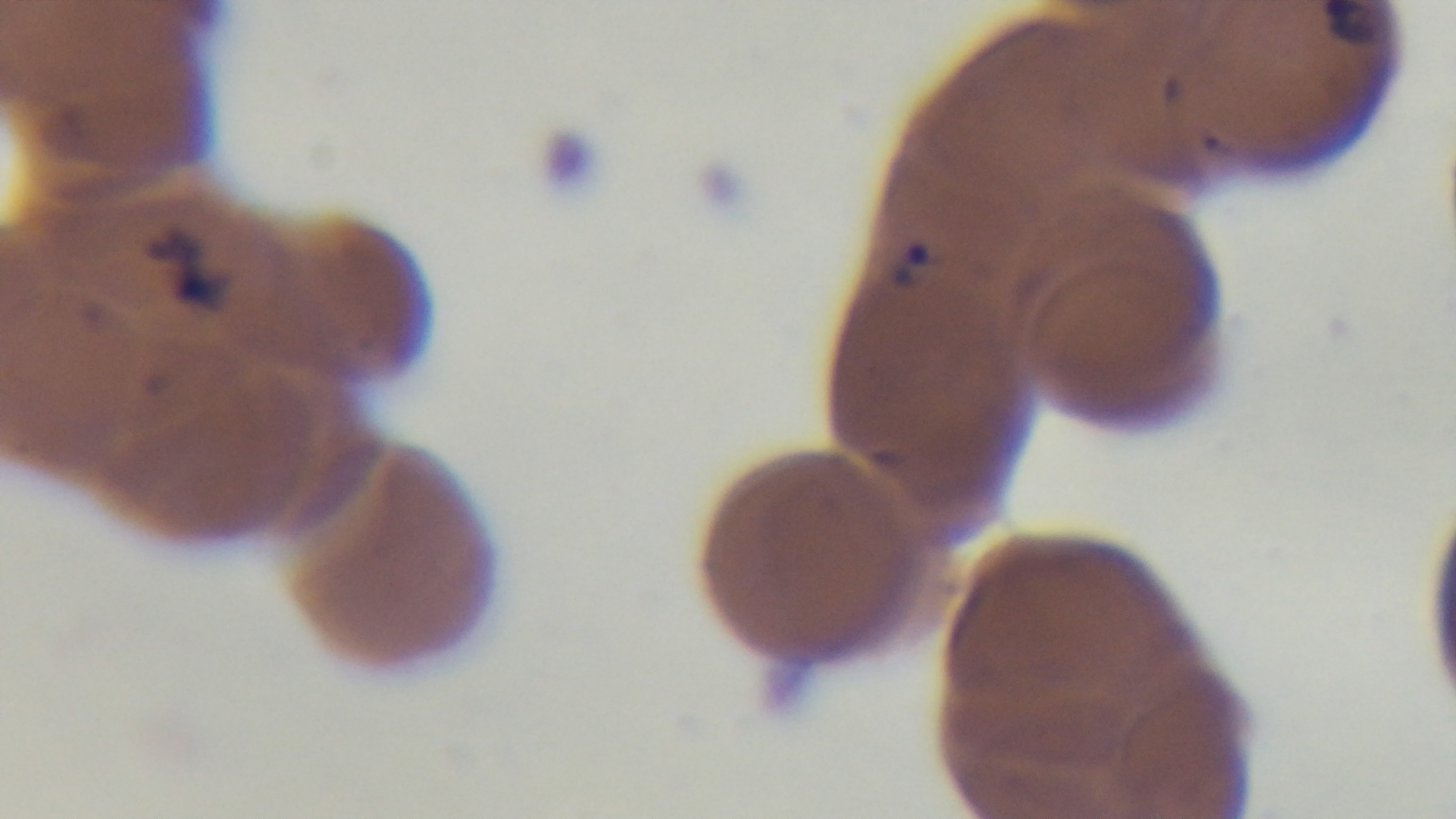
malaria status = infected
modality = light microscopy
field of view = single
preparation = thin
objective = 100x oil immersion
capture = mounted 4K digital camera
stain = Giemsa